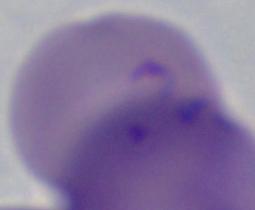
Summary:
  - Identification: Babesia
  - Modality: micrograph
  - Magnification: 1000x